Report the malaria status of this cell.
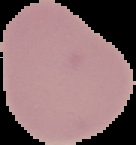
It is uninfected.

From a thin blood smear. Image is 136×145 pixels. The area outside the segmented cell region is set to black.